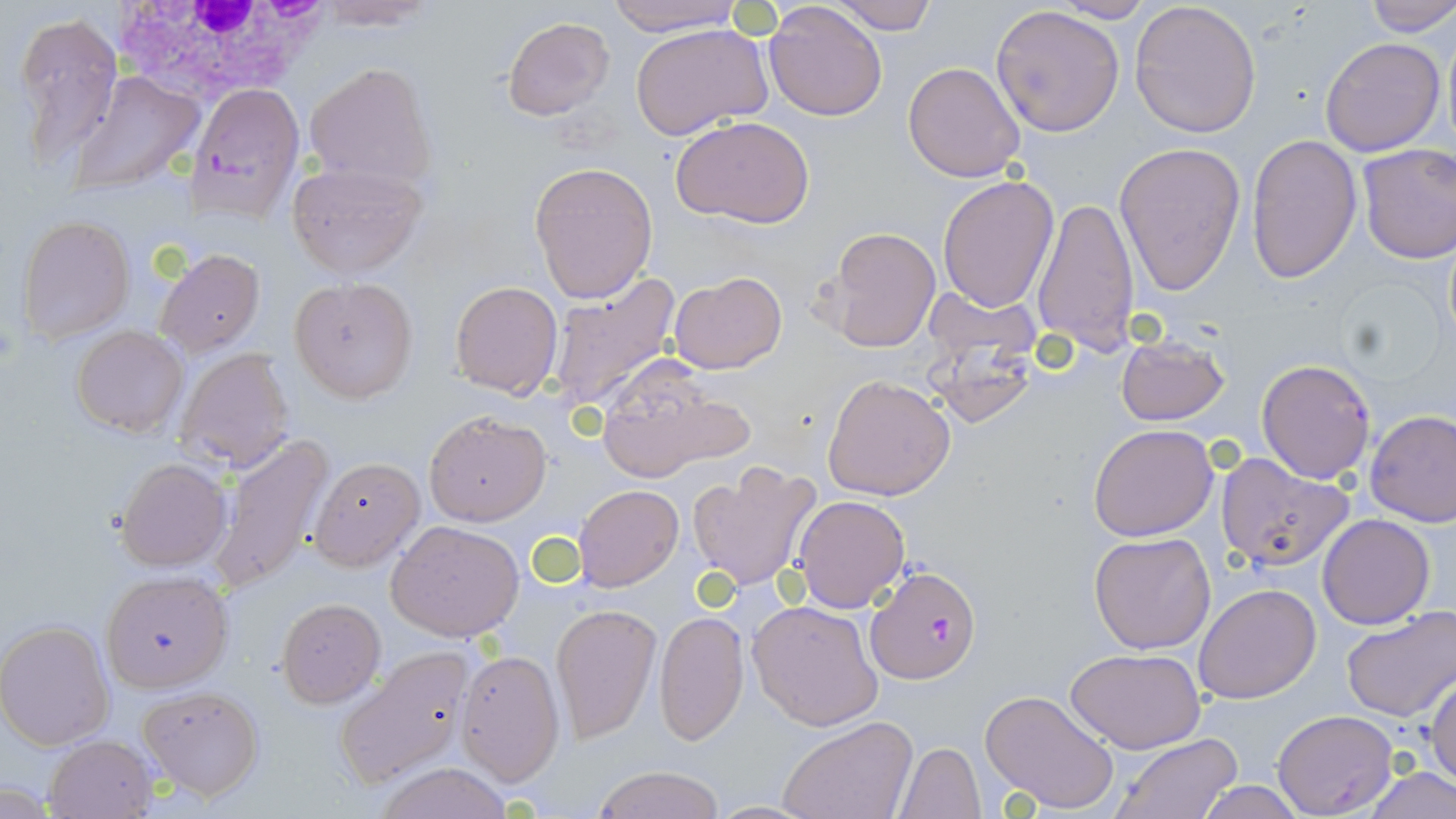

Approximate bounding boxes as [x1, y1, x2, y2] in pixels. White blood cell locations: [109, 5, 332, 92]. Plasmodium falciparum-infected red blood cell locations: [187, 83, 306, 221], [1256, 358, 1375, 483], [866, 564, 981, 683]. Uninfected red blood cell locations: [313, 0, 442, 28], [605, 0, 745, 35], [827, 0, 936, 34], [1129, 0, 1261, 140], [1359, 0, 1456, 37], [1052, 1, 1157, 23], [764, 2, 888, 120], [990, 4, 1125, 138], [12, 12, 122, 169], [500, 16, 615, 122], [629, 21, 774, 139], [1442, 22, 1456, 160], [1319, 36, 1445, 156], [304, 60, 439, 189], [902, 61, 1028, 183], [67, 71, 203, 197], [671, 115, 815, 229], [1246, 133, 1362, 283], [1113, 140, 1247, 299], [1356, 143, 1456, 263], [285, 159, 427, 278], [528, 161, 658, 303], [937, 175, 1059, 312], [1031, 196, 1142, 353], [16, 215, 136, 343], [824, 228, 941, 351], [155, 249, 265, 357], [668, 271, 787, 375], [289, 276, 418, 401], [546, 276, 680, 415], [449, 280, 563, 399], [924, 285, 1042, 373], [72, 325, 189, 437], [1115, 332, 1230, 426], [175, 347, 296, 473], [593, 358, 748, 482], [823, 374, 954, 501], [1365, 409, 1456, 527], [424, 410, 551, 525], [1088, 423, 1218, 541], [212, 434, 334, 593], [1214, 452, 1355, 572], [308, 457, 425, 571], [115, 458, 232, 571], [687, 460, 820, 592], [574, 484, 683, 591], [790, 495, 911, 611], [1317, 513, 1435, 629], [387, 521, 524, 641], [1088, 532, 1216, 654], [100, 571, 232, 694], [1195, 582, 1322, 704], [276, 598, 385, 708], [747, 598, 883, 730], [550, 604, 661, 742], [1340, 606, 1456, 721], [654, 609, 750, 745], [0, 620, 115, 749], [335, 645, 476, 788], [1066, 646, 1208, 752], [455, 648, 566, 785], [1428, 673, 1456, 791], [138, 684, 266, 798], [979, 688, 1120, 814], [1271, 710, 1398, 816], [777, 716, 918, 819], [1110, 733, 1244, 818], [46, 735, 159, 817], [895, 741, 986, 818], [370, 762, 519, 819], [1360, 765, 1456, 819], [592, 766, 725, 819], [1194, 781, 1309, 818], [706, 800, 822, 817]. Slide-level diagnosis: Plasmodium falciparum. 1000x magnification. Image is 1456×819 pixels. Thin blood film. May-Grünwald-Giemsa-stained preparation. One field of a larger specimen. Optical microscopy.